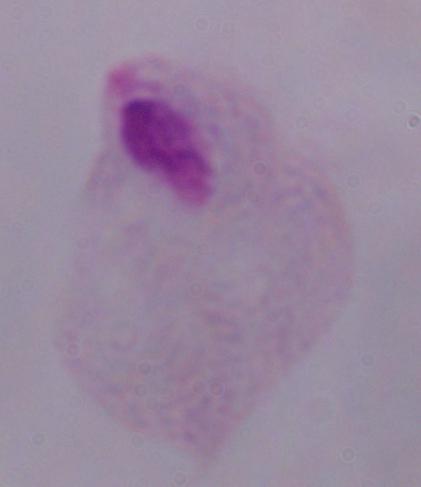

{
  "magnification": "1000x",
  "identification": "trichomonad",
  "modality": "photomicrograph"
}